Locate and identify every blood parasite.
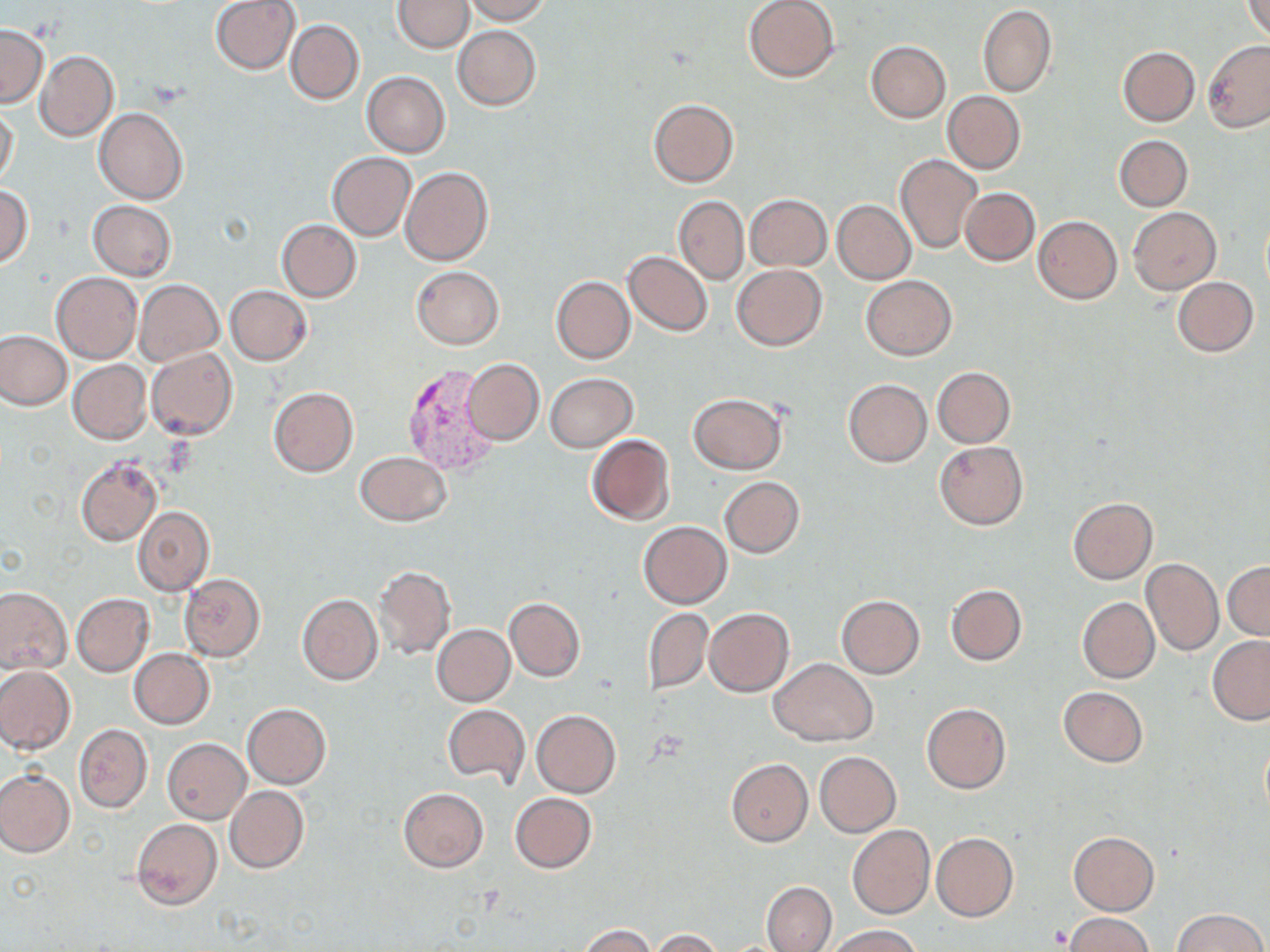

Approximate bounding boxes as (x1, y1, x2, y2) in pixels.
Plasmodium vivax-infected red blood cells: (399, 364, 497, 477).
No Plasmodium falciparum, Plasmodium ovale, Plasmodium malariae, Babesia divergens, or Trypanosoma brucei observed.

Uninfected red blood cell locations: (211, 0, 300, 74), (394, 0, 473, 52), (459, 0, 552, 24), (743, 0, 840, 83), (1241, 0, 1270, 40), (977, 4, 1055, 97), (286, 20, 364, 104), (0, 24, 47, 107), (453, 25, 542, 110), (1202, 40, 1270, 132), (865, 41, 950, 123), (1118, 46, 1200, 127), (35, 51, 118, 140), (362, 72, 450, 157), (942, 91, 1026, 174), (647, 97, 739, 187), (0, 105, 19, 188), (93, 107, 188, 204), (1115, 135, 1193, 211), (326, 152, 416, 240), (895, 153, 982, 254), (402, 168, 494, 266), (0, 187, 33, 267), (959, 187, 1039, 265), (745, 194, 831, 272), (674, 196, 748, 284), (833, 200, 915, 284), (89, 201, 176, 280), (1129, 207, 1221, 294), (1033, 215, 1122, 304), (277, 219, 361, 301), (624, 250, 713, 336), (732, 264, 828, 350), (411, 266, 503, 349), (52, 273, 142, 364), (861, 275, 957, 359), (551, 276, 635, 364), (1172, 277, 1258, 356), (135, 279, 223, 365), (225, 285, 312, 365), (0, 330, 73, 410), (147, 347, 238, 439), (462, 358, 544, 445), (68, 360, 152, 444), (464, 365, 633, 443), (931, 367, 1016, 448), (545, 373, 637, 451), (843, 379, 931, 467), (268, 387, 359, 477), (687, 393, 788, 474), (585, 434, 676, 526), (933, 440, 1028, 530), (354, 451, 451, 527), (74, 456, 162, 547), (719, 477, 805, 559), (1067, 497, 1158, 584), (132, 505, 214, 597), (638, 521, 732, 609), (1142, 558, 1223, 656), (1223, 561, 1270, 639), (374, 565, 456, 659), (178, 573, 266, 661), (946, 584, 1027, 665), (0, 586, 72, 675), (72, 593, 154, 675), (297, 594, 383, 686), (836, 595, 926, 678), (1077, 596, 1159, 684), (505, 597, 584, 681), (704, 607, 794, 696), (644, 608, 713, 693), (432, 624, 514, 706), (1208, 636, 1270, 724), (129, 648, 214, 729), (769, 658, 876, 745), (0, 665, 75, 756), (1057, 686, 1147, 767), (242, 703, 330, 788), (922, 703, 1011, 794), (442, 705, 531, 788), (532, 710, 621, 797), (74, 723, 153, 813), (1259, 735, 1269, 821), (163, 738, 250, 823), (814, 751, 901, 836), (726, 757, 813, 846), (0, 770, 74, 857), (225, 785, 308, 874), (398, 787, 489, 872), (509, 792, 597, 873), (132, 817, 222, 910), (847, 825, 935, 919), (1069, 831, 1159, 915), (931, 833, 1018, 923), (762, 881, 836, 952), (1174, 908, 1266, 952), (1065, 913, 1154, 952), (580, 924, 655, 952), (829, 925, 920, 952), (651, 928, 725, 951). Slide-level diagnosis: Plasmodium vivax. Image is 1270×952 pixels. Light microscopy. May-Grünwald-Giemsa stain. Thin blood film. Captured at 1000x magnification. One field of a larger specimen.